Identify the parasite.
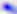
This is Toxoplasma gondii.

Summary:
  - Modality: photomicrograph
  - Magnification: 400x